Assess the morphology of the erythrocytes.
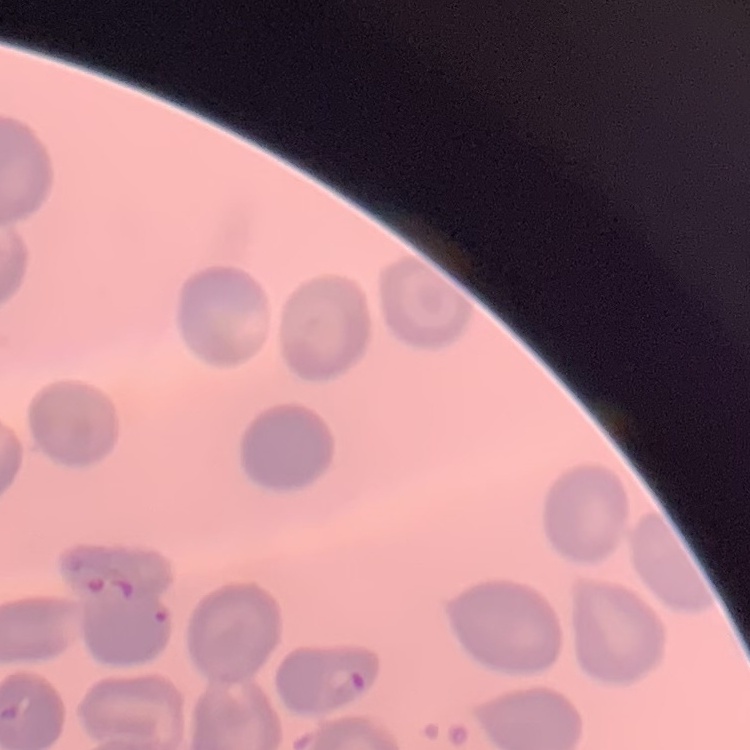

No rouleaux formation.

Square crop of a larger photomicrograph. Thin blood smear. Field's or Giemsa stain.